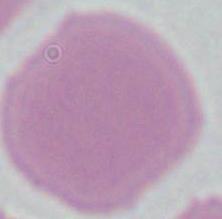
{
  "modality": "photomicrograph",
  "magnification": "1000x",
  "identification": "erythrocyte"
}